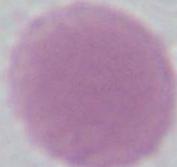
magnification = 1000x
modality = micrograph
identification = red blood cell